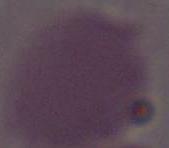

Micrograph. A red blood cell is shown. 1000x magnification.